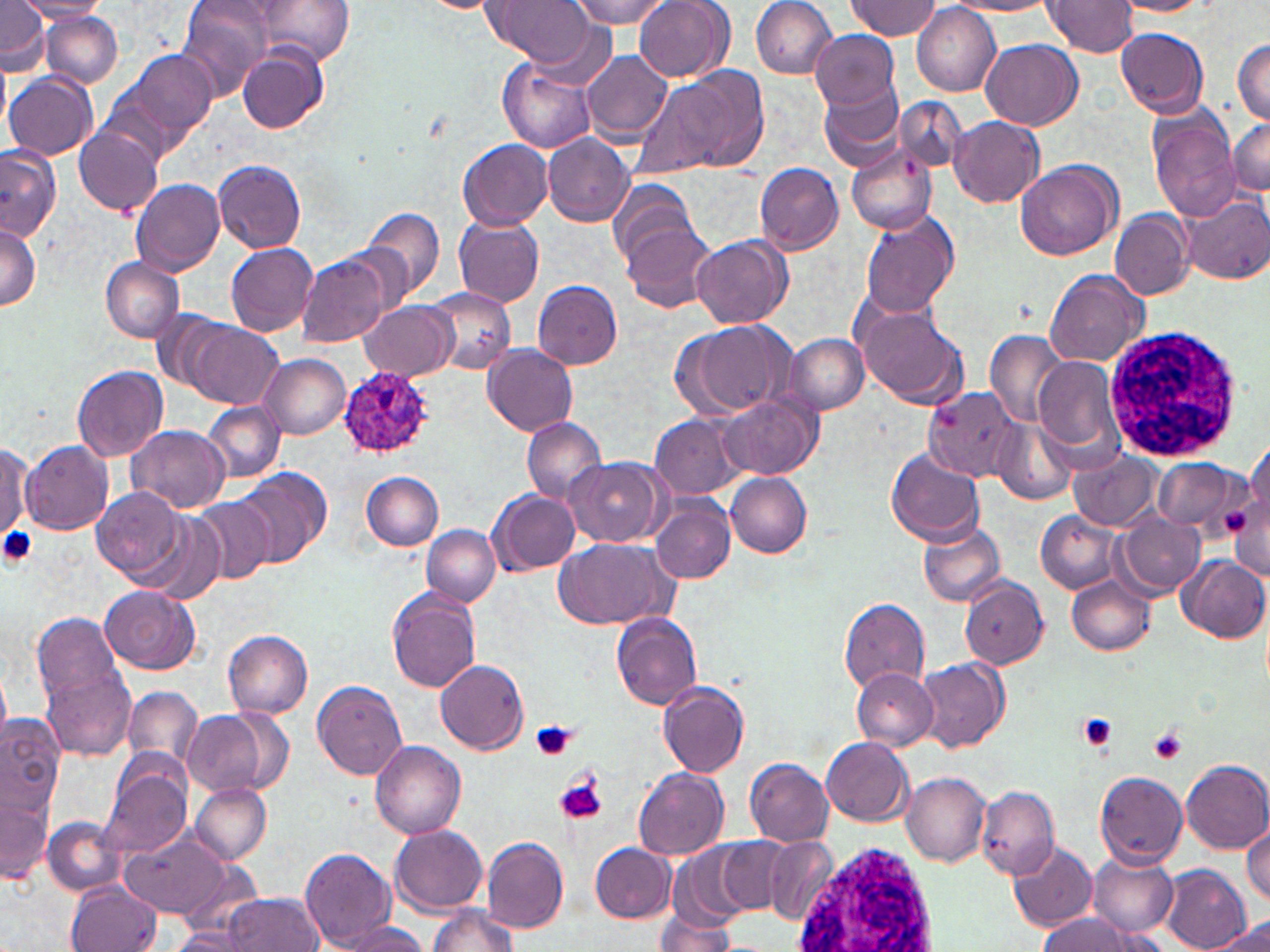
Summary:
  - Coordinate format: approximate bounding boxes as (x1, y1, x2, y2) in pixels
  - Uninfected red blood cell locations: (16, 0, 110, 20), (179, 0, 274, 101), (259, 0, 353, 65), (570, 0, 669, 28), (635, 0, 733, 81), (751, 0, 839, 78), (1042, 0, 1138, 57), (1115, 0, 1213, 16), (0, 1, 50, 76), (489, 1, 600, 70), (847, 1, 941, 39), (950, 1, 1059, 15), (911, 4, 1000, 98), (43, 11, 123, 88), (1114, 28, 1210, 116), (810, 29, 900, 109), (981, 39, 1082, 130), (1232, 39, 1270, 124), (237, 46, 326, 133), (118, 50, 219, 151), (580, 50, 673, 143), (497, 56, 597, 153), (0, 61, 11, 137), (649, 67, 767, 175), (5, 73, 98, 160), (818, 82, 907, 173), (893, 97, 966, 172), (1149, 107, 1242, 223), (949, 116, 1044, 208), (1228, 117, 1270, 195), (75, 124, 163, 217), (543, 134, 634, 227), (458, 138, 551, 230), (0, 144, 62, 241), (846, 145, 938, 236), (1015, 159, 1122, 260), (214, 160, 307, 252), (755, 163, 843, 254), (131, 178, 226, 276), (607, 180, 698, 269), (1179, 195, 1269, 284), (363, 207, 445, 301), (1109, 209, 1193, 300), (859, 210, 960, 318), (455, 217, 545, 306), (621, 220, 718, 313), (0, 224, 40, 311), (691, 235, 791, 327), (226, 242, 319, 335), (296, 254, 390, 347), (100, 257, 184, 341), (1045, 269, 1150, 365), (533, 280, 623, 369), (426, 287, 515, 375), (359, 300, 455, 381), (854, 300, 970, 409), (179, 319, 282, 409), (674, 319, 796, 420), (984, 331, 1066, 424), (784, 332, 869, 415), (485, 344, 579, 435), (260, 354, 350, 438), (1032, 358, 1123, 454), (72, 364, 169, 461), (924, 387, 1020, 480), (722, 397, 818, 480), (202, 402, 286, 483), (651, 413, 746, 501), (521, 417, 606, 504), (993, 420, 1076, 504), (126, 426, 232, 513), (1244, 437, 1269, 533), (20, 440, 114, 534), (1, 441, 33, 545), (886, 449, 987, 546), (1070, 452, 1161, 530), (1154, 457, 1244, 533), (564, 458, 668, 546), (235, 468, 329, 568), (361, 471, 443, 551), (726, 473, 813, 557), (91, 485, 187, 582), (489, 491, 579, 574), (192, 495, 276, 584), (650, 497, 735, 584), (1036, 510, 1122, 594), (138, 514, 228, 604), (1115, 514, 1205, 597), (917, 521, 1007, 608), (421, 525, 499, 606), (554, 537, 671, 628), (1177, 555, 1269, 643), (1067, 574, 1155, 656), (959, 579, 1048, 668), (100, 586, 201, 673), (388, 589, 481, 693), (840, 598, 931, 692), (31, 611, 125, 706), (612, 613, 702, 709), (221, 629, 313, 719), (917, 659, 1009, 752), (436, 660, 528, 753), (42, 665, 136, 761), (0, 667, 10, 746), (852, 668, 939, 750), (312, 680, 406, 781), (659, 681, 749, 777), (122, 687, 201, 769), (181, 710, 272, 796), (0, 716, 64, 821), (821, 737, 914, 826), (370, 738, 467, 839), (745, 758, 833, 846), (1181, 758, 1270, 852), (99, 761, 192, 858), (632, 767, 729, 860), (1093, 770, 1188, 869), (902, 773, 990, 865), (189, 781, 271, 864), (975, 785, 1059, 881), (0, 787, 53, 885), (44, 818, 123, 896), (1245, 820, 1270, 907), (390, 822, 489, 915), (122, 829, 231, 922), (483, 837, 569, 932), (765, 838, 840, 924), (720, 839, 791, 912), (1009, 840, 1099, 933), (589, 842, 675, 923), (667, 844, 755, 928), (299, 848, 398, 952), (1086, 853, 1178, 937), (1160, 865, 1252, 952), (67, 879, 161, 952), (222, 892, 324, 951), (428, 904, 518, 952), (653, 912, 738, 951), (1036, 913, 1150, 951), (1211, 918, 1270, 951), (333, 921, 432, 952), (167, 926, 256, 951)
  - Platelet locations: (0, 527, 39, 569), (1077, 713, 1119, 751), (531, 721, 577, 761), (1148, 729, 1187, 766), (556, 776, 606, 825)
  - Plasmodium ovale-infected red blood cell locations: (339, 366, 435, 460)
  - White blood cell locations: (1100, 324, 1245, 462), (791, 843, 943, 952)
  - Slide-level diagnosis: Plasmodium ovale
  - Image size: 1270×952 pixels
  - Stain: May-Grünwald-Giemsa
  - Preparation: thin blood smear
  - Magnification: 1000x
  - Modality: light microscopy
  - Field of view: single